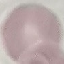
Malaria status: uninfected. Photographed with a smartphone camera at the microscope eyepiece. Thin blood smear. Cell patch, automatically extracted from a larger field of view and resized to 64 × 64 pixels. Giemsa stain.